Identify the parasite.
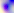

Toxoplasma gondii.

{
  "magnification": "400x",
  "modality": "micrograph"
}